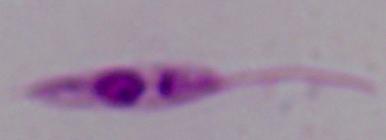

1000x magnification. Micrograph. A Leishmania parasite is seen.